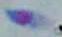

Summary:
  - Magnification: 1000x
  - Identification: Toxoplasma gondii
  - Modality: micrograph